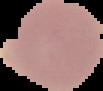 Result: no malaria parasites seen. From a thin blood film. Image is 103×91 pixels. The area outside the segmented cell region is set to black.